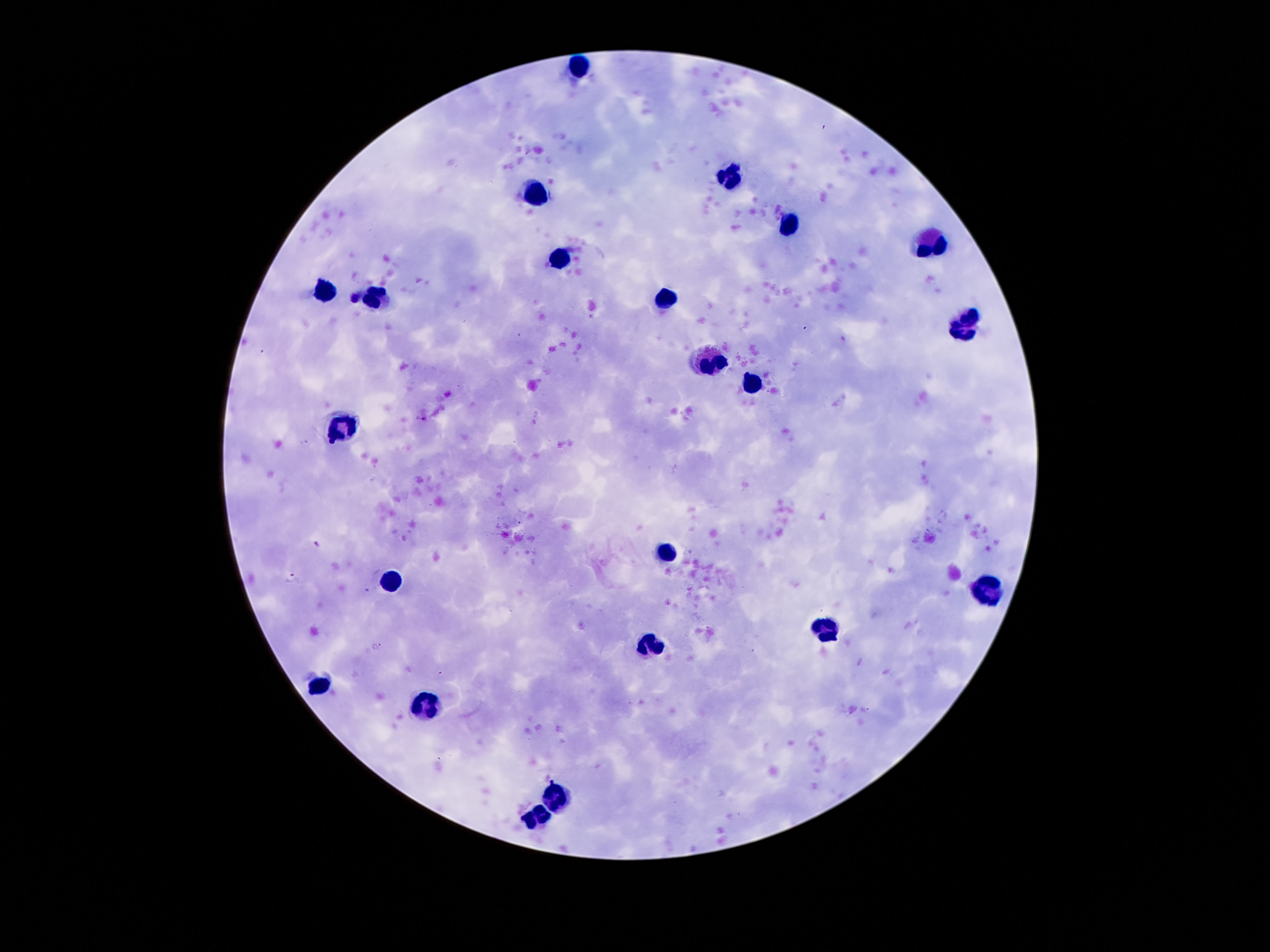

Approximate object centers, in pixels from the top-left corner.
Summary:
  - Leukocyte locations: (x=578, y=64), (x=729, y=177), (x=535, y=197), (x=787, y=222), (x=932, y=243), (x=557, y=261), (x=326, y=290), (x=371, y=300), (x=666, y=300), (x=963, y=327), (x=709, y=361), (x=754, y=382), (x=340, y=429), (x=668, y=550), (x=389, y=581), (x=993, y=591), (x=825, y=632), (x=653, y=644), (x=318, y=687), (x=430, y=702), (x=557, y=796), (x=535, y=818)
  - Preparation: thick peripheral-blood smear
  - Field of view: single
  - Magnification: 100x
  - Capture: smartphone camera through the microscope eyepiece
  - Stain: Giemsa
  - Image size: 1270×952 pixels
  - Patient malaria status: uninfected